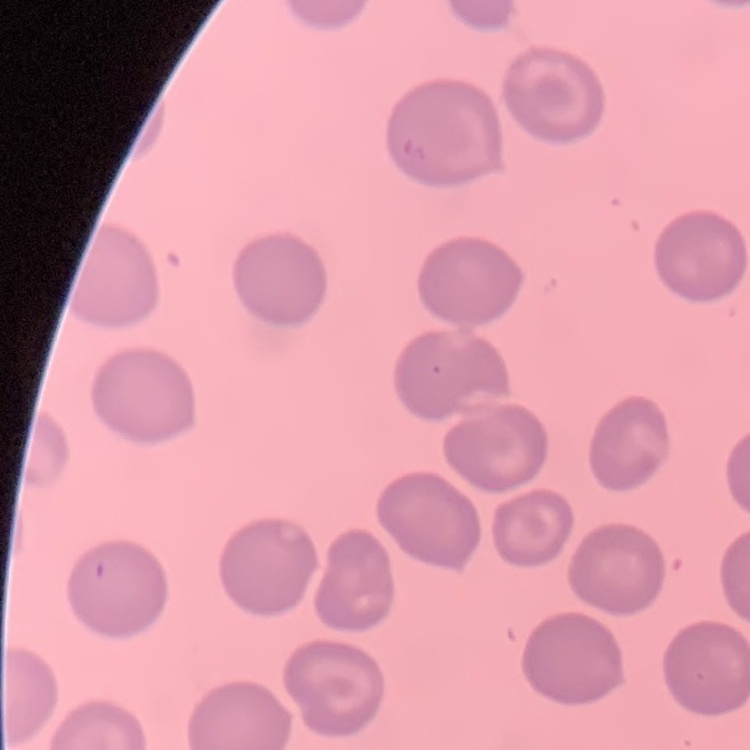
{
  "erythrocyte_morphology": "no rouleaux formation",
  "stain": "Field's or Giemsa",
  "preparation": "thin blood smear",
  "image_type": "square crop of a larger photomicrograph"
}